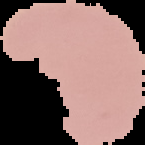

{
  "result": "no malaria parasites seen",
  "image_type": "cell region segmented out of the field of view; surrounding area masked to black",
  "image_size": "145×145 pixels",
  "preparation": "thin blood smear"
}